Report the malaria status of this cell.
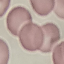

It is uninfected.

stain = Giemsa
image type = cell patch, automatically extracted from a larger field of view and resized to 64 × 64 pixels
preparation = thin blood smear
capture = smartphone camera at the microscope eyepiece